Outline each uninfected red blood cell.
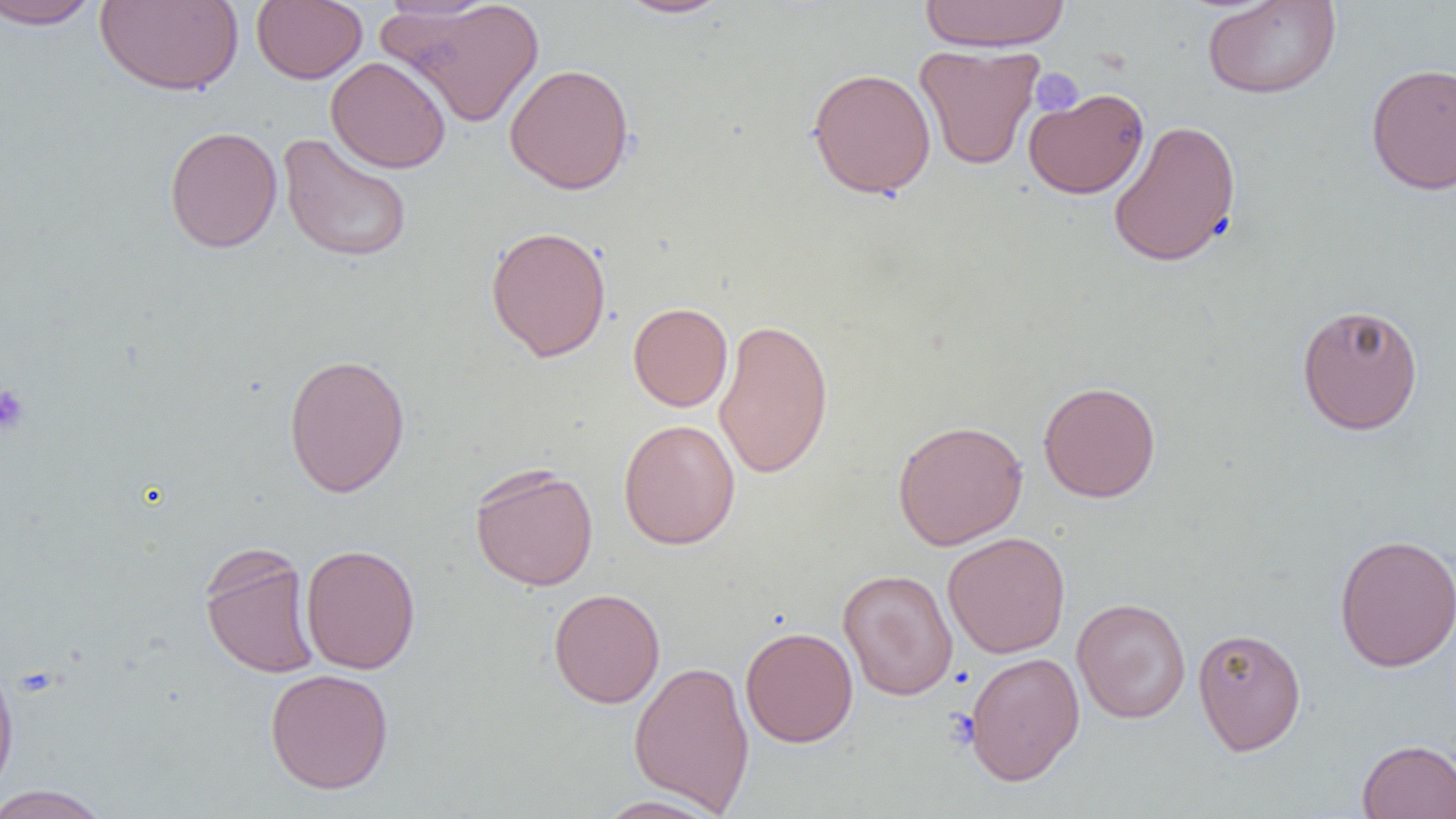
Approximate bounding boxes as (x1, y1, x2, y2) in pixels.
Uninfected red blood cells: (0, 0, 106, 31), (251, 0, 367, 84), (375, 0, 501, 22), (380, 0, 545, 128), (615, 0, 733, 19), (920, 0, 1070, 51), (1202, 0, 1341, 99), (94, 1, 244, 95), (914, 44, 1043, 170), (326, 56, 452, 174), (1365, 62, 1456, 195), (504, 63, 635, 195), (807, 67, 936, 199), (1024, 86, 1149, 199), (1108, 119, 1241, 268), (164, 126, 283, 253), (278, 133, 413, 264), (485, 225, 612, 362), (628, 302, 733, 411), (1296, 303, 1424, 436), (713, 317, 834, 479), (283, 352, 411, 498), (1038, 380, 1162, 503), (618, 419, 740, 550), (892, 419, 1029, 550), (469, 463, 599, 591), (942, 531, 1071, 658), (1333, 533, 1456, 673), (288, 543, 407, 794), (300, 543, 421, 675), (199, 544, 321, 679), (838, 569, 958, 701), (549, 588, 665, 708), (1072, 597, 1191, 724), (740, 626, 858, 747), (1192, 626, 1306, 755), (963, 651, 1085, 785), (0, 659, 20, 801), (629, 659, 755, 814), (265, 668, 394, 795), (1357, 739, 1456, 818), (0, 784, 114, 819), (592, 795, 728, 818).

Platelet locations: (1030, 68, 1084, 117), (0, 383, 31, 436), (944, 708, 980, 751). Slide-level diagnosis: negative for blood parasites. Image is 1456×819 pixels. 1000x magnification. Light microscopy. One field of a larger specimen. Thin blood film.